Name the parasite shown.
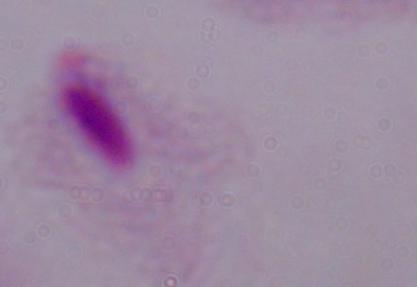
A trichomonad.

Summary:
  - Modality: micrograph
  - Magnification: 1000x